Assess the morphology of the red blood cells.
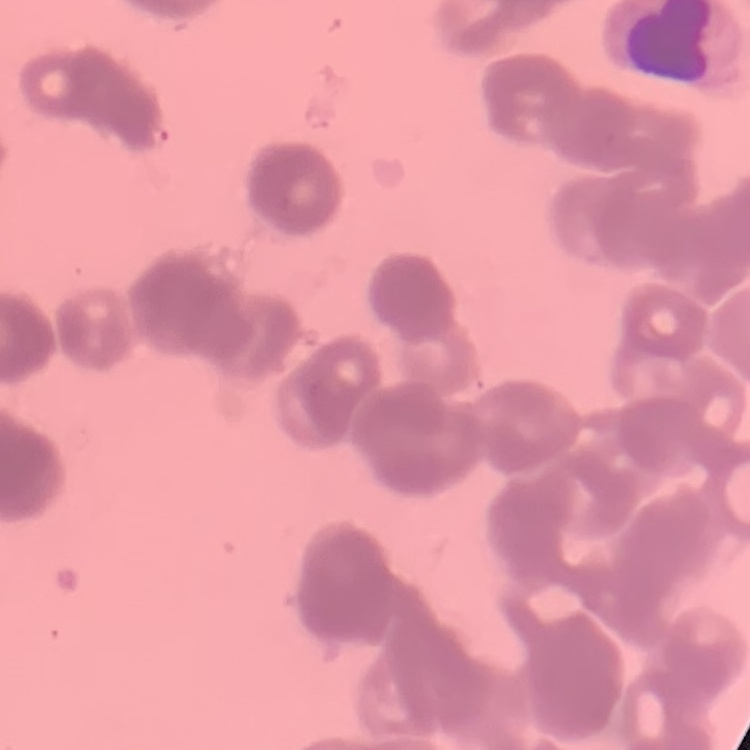

They show rouleaux formation.

One tile cut from a larger photomicrograph. Field's or Giemsa stain. Thin peripheral smear.